Classify this cell by malaria status.
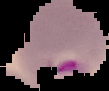
Parasitized.

preparation = thin blood film
image size = 109×91 pixels
image type = segmented cell region on a black background